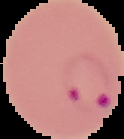

image type = segmented cell region on a black background
image size = 124×139 pixels
preparation = thin blood film
malaria status = parasitized